Assess this cell for malaria.
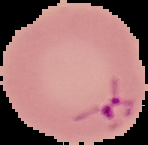

It is parasitized.

Summary:
  - Image size: 148×145 pixels
  - Preparation: thin blood smear
  - Image type: segmented cell region on a black background